Locate every P. falciparum parasite and give its life-cycle stage, and locate every leukocyte and any debris.
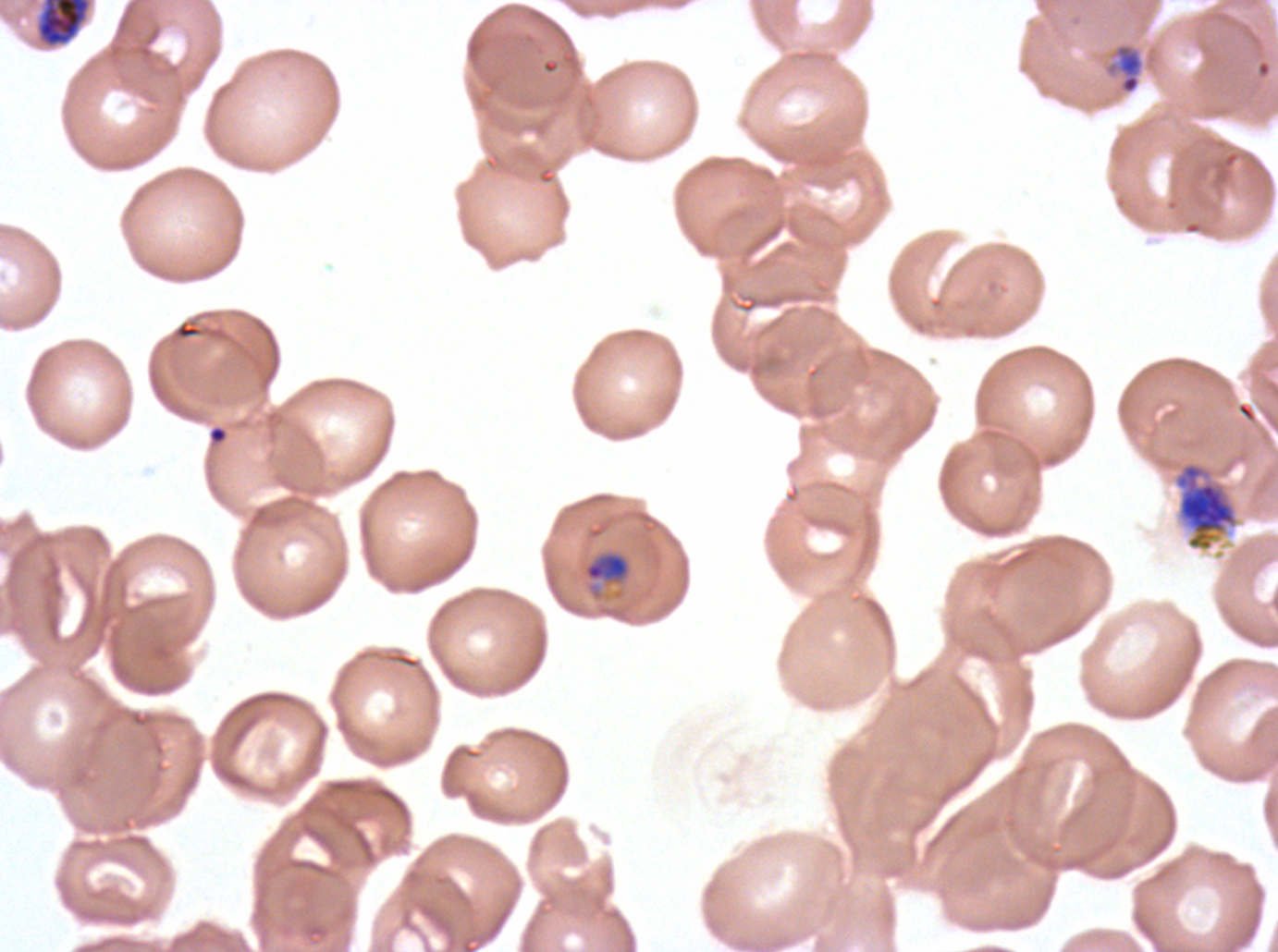
Approximate bounding rectangles given as corner coordinates in pixels from the top-left.
Rings: (x1=208, y1=425, x2=227, y2=444).
Late-ring/early-trophozoite forms: (x1=1106, y1=43, x2=1144, y2=95).
Mid trophozoites: (x1=584, y1=553, x2=629, y2=581).
Late trophozoites: (x1=37, y1=0, x2=90, y2=46), (x1=1174, y1=461, x2=1238, y2=552).
No early schizonts, late schizonts, segmenters, gametocytes, leukocytes, or debris observed.

field of view = one sub-image of a larger composite
specimen = P. falciparum from a patient in The Gambia, cultured ex vivo for 24 to 48 hours
image size = 1278×952 pixels
stain = Giemsa
preparation = thin blood film
life-cycle stages observed = ring, late-ring/early-trophozoite, mid trophozoite, late trophozoite